Assess this cell for malaria.
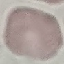

It is uninfected.

Thin smear of blood. Automatically extracted cell patch, resized to 64 × 64 pixels. Giemsa-stained preparation. Acquired by smartphone through the microscope eyepiece.